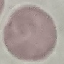
Summary:
  - Result: no malaria parasites seen
  - Image type: automatically extracted cell patch, resized to 64 × 64 pixels
  - Preparation: thin blood smear
  - Stain: Giemsa
  - Capture: smartphone through the microscope eyepiece